State which parasite is depicted.
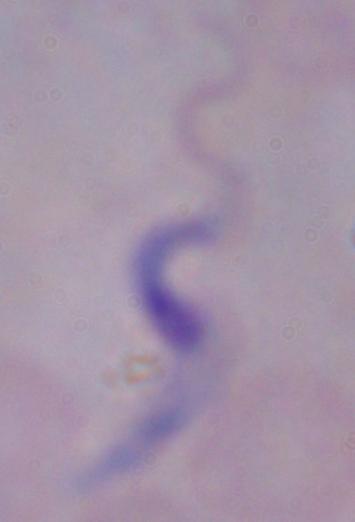
A trypanosome.

{
  "modality": "micrograph",
  "magnification": "1000x"
}